Locate every malaria parasite.
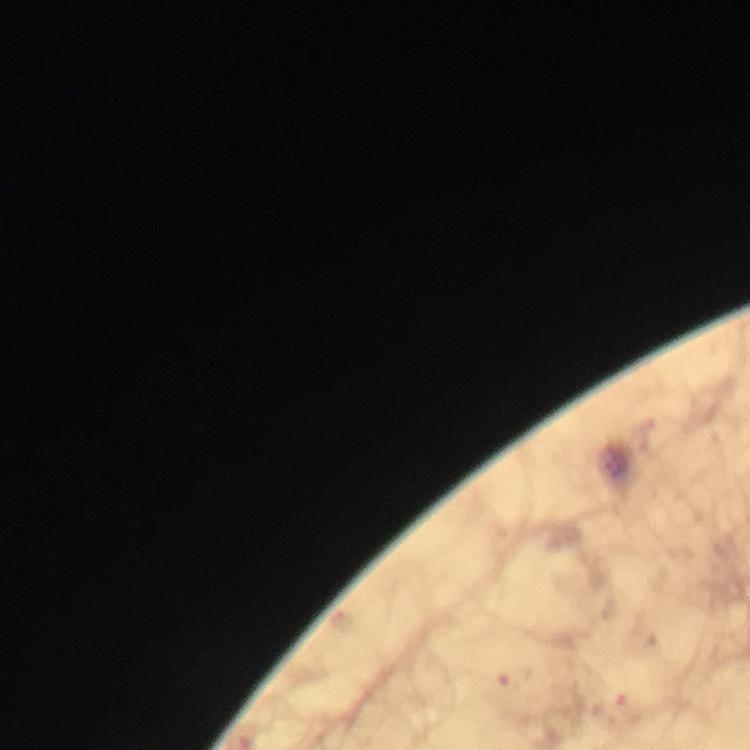

Approximate centers as {x, y} in pixels.
Malaria parasites: {516, 677}.

context = from a malaria diagnostic workup
image size = 750×750 pixels
preparation = thick smear
immersion oil = used
stain = Giemsa
capture = smartphone camera through the microscope
magnification = 100x
cropped from = a single field of view